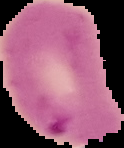
Summary:
  - Preparation: thin blood film
  - Malaria status: parasitized
  - Image size: 124×148 pixels
  - Image type: segmented cell region with the area outside set to black